Locate every Babesia divergens-infected red blood cell.
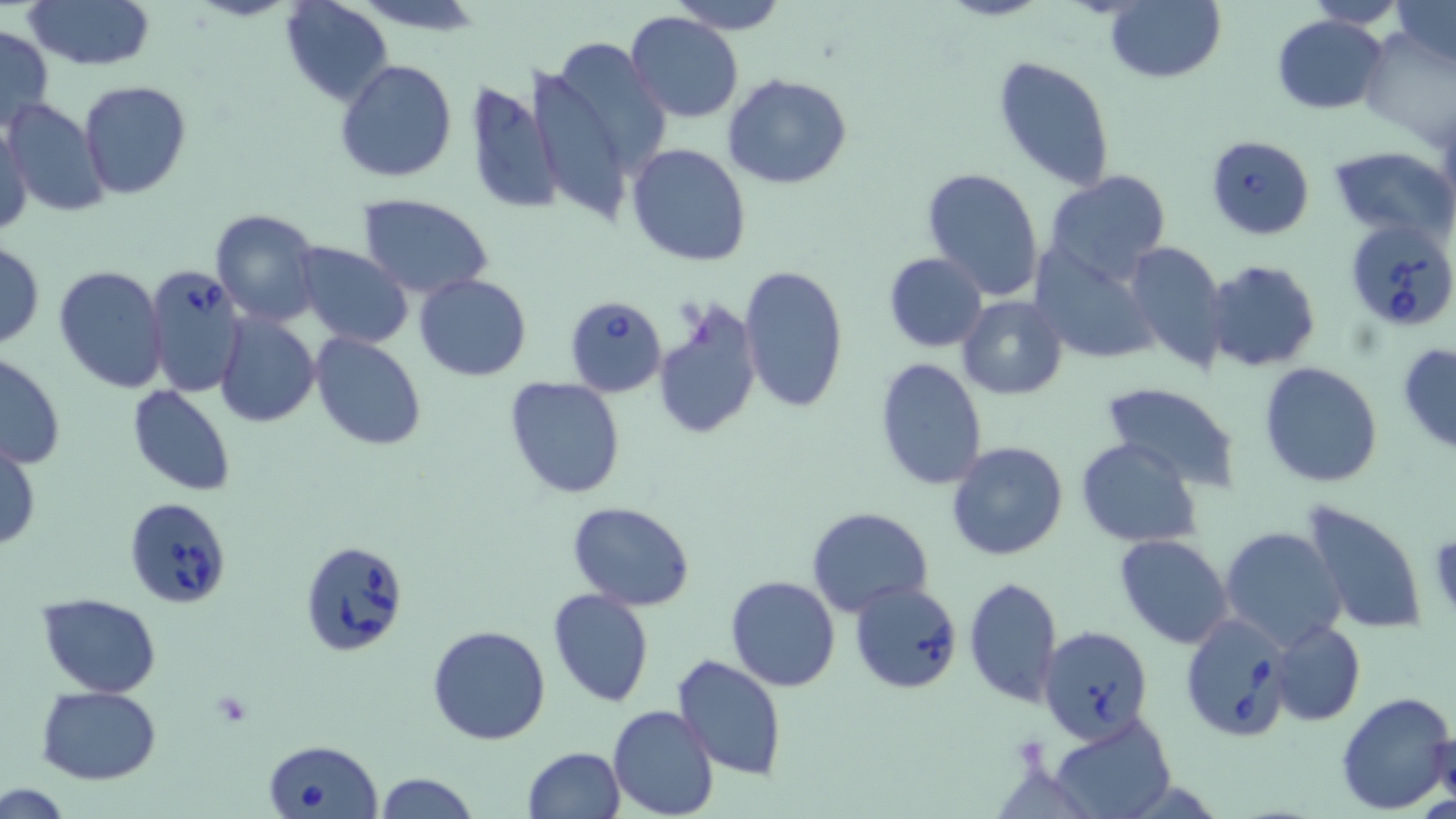

Approximate bounding boxes as (x1, y1, x2, y2) in pixels.
Babesia divergens-infected red blood cells: (1206, 134, 1315, 240), (1347, 220, 1453, 335), (145, 263, 247, 398), (563, 294, 668, 398), (123, 496, 232, 609), (299, 539, 410, 656), (848, 579, 963, 694), (1178, 612, 1294, 741), (1037, 626, 1153, 743), (261, 738, 382, 818).

{
  "slide_level_diagnosis": "Babesia divergens",
  "field_of_view": "single",
  "preparation": "thin blood film",
  "image_size": "1456×819 pixels",
  "modality": "optical microscopy",
  "magnification": "1000x",
  "stain": "May-Grünwald-Giemsa",
  "uninfected_red_blood_cell_locations": "approximate bounding boxes as (x1, y1, x2, y2) in pixels: (21, 0, 154, 71), (281, 0, 394, 106), (669, 0, 788, 34), (1106, 0, 1225, 84), (1303, 0, 1411, 27), (1391, 0, 1456, 69), (626, 12, 745, 124), (1272, 15, 1387, 114), (0, 24, 53, 134), (1358, 29, 1452, 144), (529, 39, 667, 218), (992, 57, 1114, 192), (334, 60, 458, 184), (723, 73, 852, 190), (465, 80, 565, 218), (79, 81, 192, 200), (3, 98, 110, 219), (0, 121, 32, 238), (626, 143, 751, 268), (1328, 144, 1454, 241), (921, 167, 1044, 302), (1043, 169, 1173, 285), (357, 194, 494, 300), (209, 209, 324, 326), (0, 240, 44, 349), (1123, 241, 1228, 373), (1027, 242, 1158, 366), (290, 243, 411, 349), (883, 252, 987, 351), (1207, 261, 1320, 372), (54, 265, 169, 395), (738, 266, 847, 413), (414, 274, 531, 381), (956, 295, 1067, 400), (654, 301, 763, 441), (214, 314, 321, 427), (311, 333, 425, 452), (1397, 342, 1456, 453), (0, 352, 67, 470), (874, 358, 989, 491), (1259, 362, 1383, 487), (504, 376, 628, 499), (1100, 382, 1245, 493), (127, 384, 237, 496), (1076, 437, 1203, 548), (1, 439, 40, 552), (946, 441, 1070, 563), (1300, 500, 1429, 635), (568, 501, 696, 610), (806, 507, 933, 617), (1219, 525, 1347, 651), (1115, 534, 1233, 648), (724, 575, 842, 692), (963, 576, 1063, 706), (546, 588, 655, 708), (37, 593, 161, 697), (1269, 620, 1366, 726), (428, 625, 551, 747), (671, 654, 788, 781), (36, 686, 161, 783), (1335, 690, 1456, 812), (609, 704, 718, 819), (1048, 713, 1176, 819), (1434, 729, 1456, 812), (523, 745, 626, 818), (373, 772, 481, 819), (1, 784, 76, 817)"
}